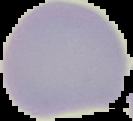
From a thin blood film. Image is 133×121 pixels. Result: no Plasmodium parasites detected. Segmented cell region on a black background.